Classify this cell by malaria status.
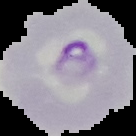

It is parasitized.

Summary:
  - Image size: 136×136 pixels
  - Preparation: thin blood smear
  - Image type: segmented cell region on a black background